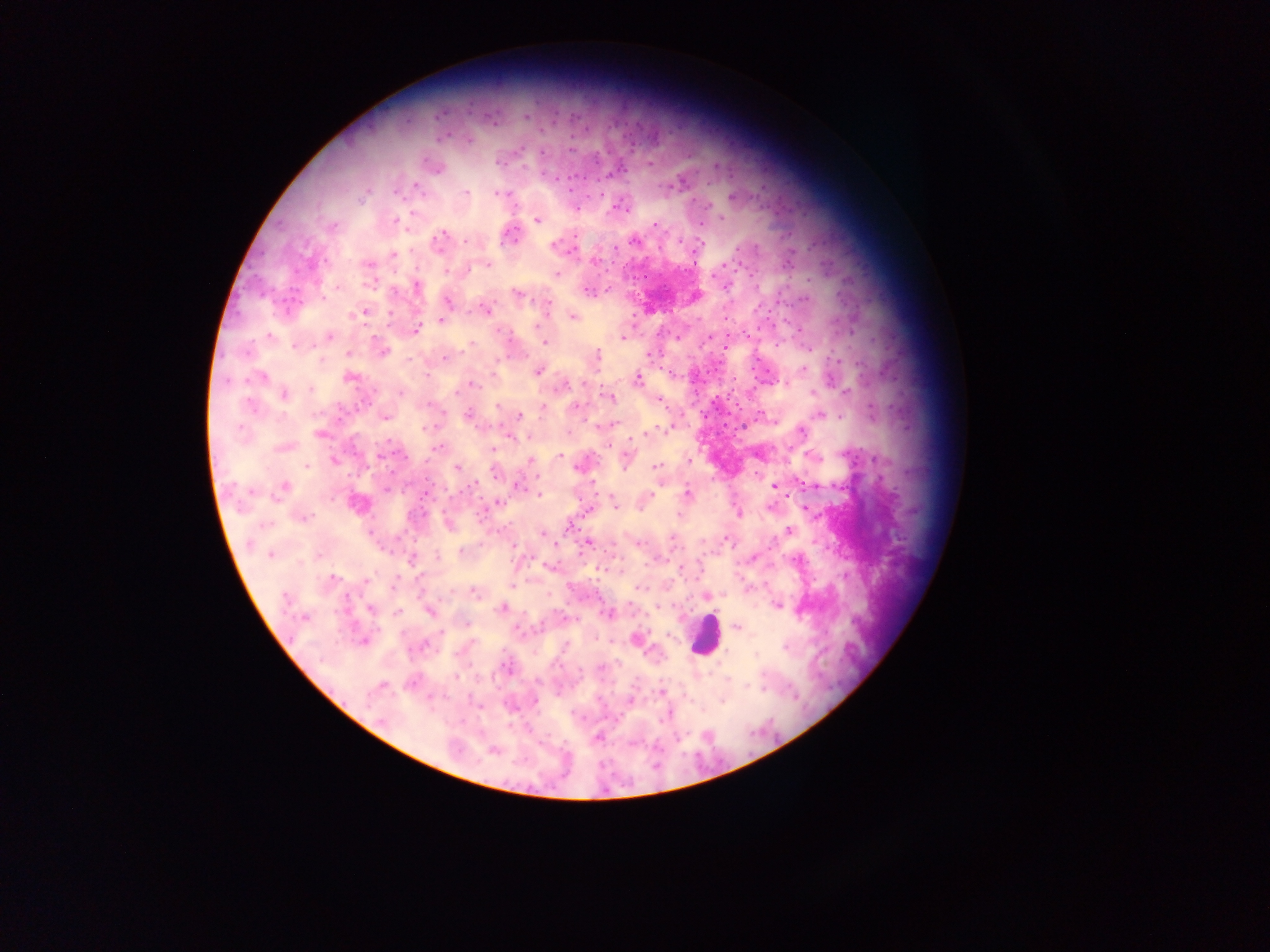

Approximate centers as [x, y] in pixels. Plasmodium parasite locations: [527, 116], [468, 139], [542, 152], [649, 163], [434, 166], [681, 180], [416, 186], [465, 193], [500, 193], [506, 194], [733, 197], [576, 209], [721, 218], [538, 219], [394, 221], [701, 224], [332, 225], [656, 225], [510, 236], [439, 241], [467, 241], [634, 241], [554, 246], [571, 250], [393, 255], [594, 261], [368, 265], [486, 265], [557, 274], [371, 282], [726, 285], [415, 286], [588, 291], [518, 293], [694, 296], [447, 300], [486, 310], [361, 313], [572, 315], [442, 320], [416, 329], [624, 336], [328, 337], [545, 342], [382, 351], [648, 353], [596, 355], [804, 369], [538, 370], [259, 376], [350, 376], [637, 380], [473, 383], [787, 383], [564, 384], [284, 394], [609, 395], [659, 400], [496, 406], [543, 407], [576, 407], [821, 414], [468, 415], [384, 416], [520, 416], [614, 422], [603, 424], [801, 431], [320, 434], [509, 436], [283, 447], [438, 448], [493, 449], [758, 453], [559, 456], [811, 456], [625, 458], [334, 460], [530, 461], [581, 466], [656, 466], [457, 467], [495, 472], [474, 485], [517, 485], [774, 486], [386, 488], [283, 489], [424, 494], [687, 494], [538, 495], [648, 496], [496, 502], [357, 503], [613, 503], [738, 514], [302, 517], [448, 523], [569, 525], [789, 530], [543, 534], [726, 538], [587, 542], [511, 544], [461, 551], [270, 554], [438, 556], [752, 557], [412, 559], [550, 566], [513, 585], [638, 587], [476, 591], [706, 596], [778, 605], [502, 608], [371, 609], [430, 611], [397, 613], [607, 613], [464, 623], [737, 627], [636, 639], [363, 640], [756, 654], [505, 667], [661, 691], [723, 699], [630, 700], [534, 702], [596, 738], [493, 750]. Leukocyte locations: [704, 636]. Image is 1270×952 pixels. Thick blood film. Collected in Ghana. Mobile-phone photograph taken through the microscope. Single field of view.